Assess this cell for malaria.
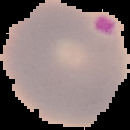
It is parasitized.

image_size: 130×130 pixels
image_type: segmented cell region on a black background
preparation: thin blood film